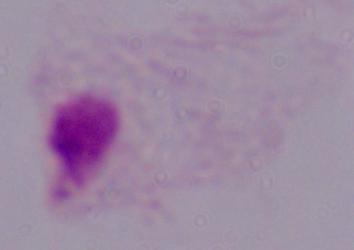

Photomicrograph. A trichomonad is shown. 1000x magnification.